Report the malaria status of this cell.
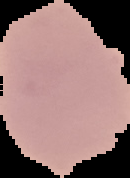
Uninfected.

Image is 130×178 pixels. From a thin blood smear. The area outside the segmented cell region is set to black.